Give the extent of all uninfected red blood cells.
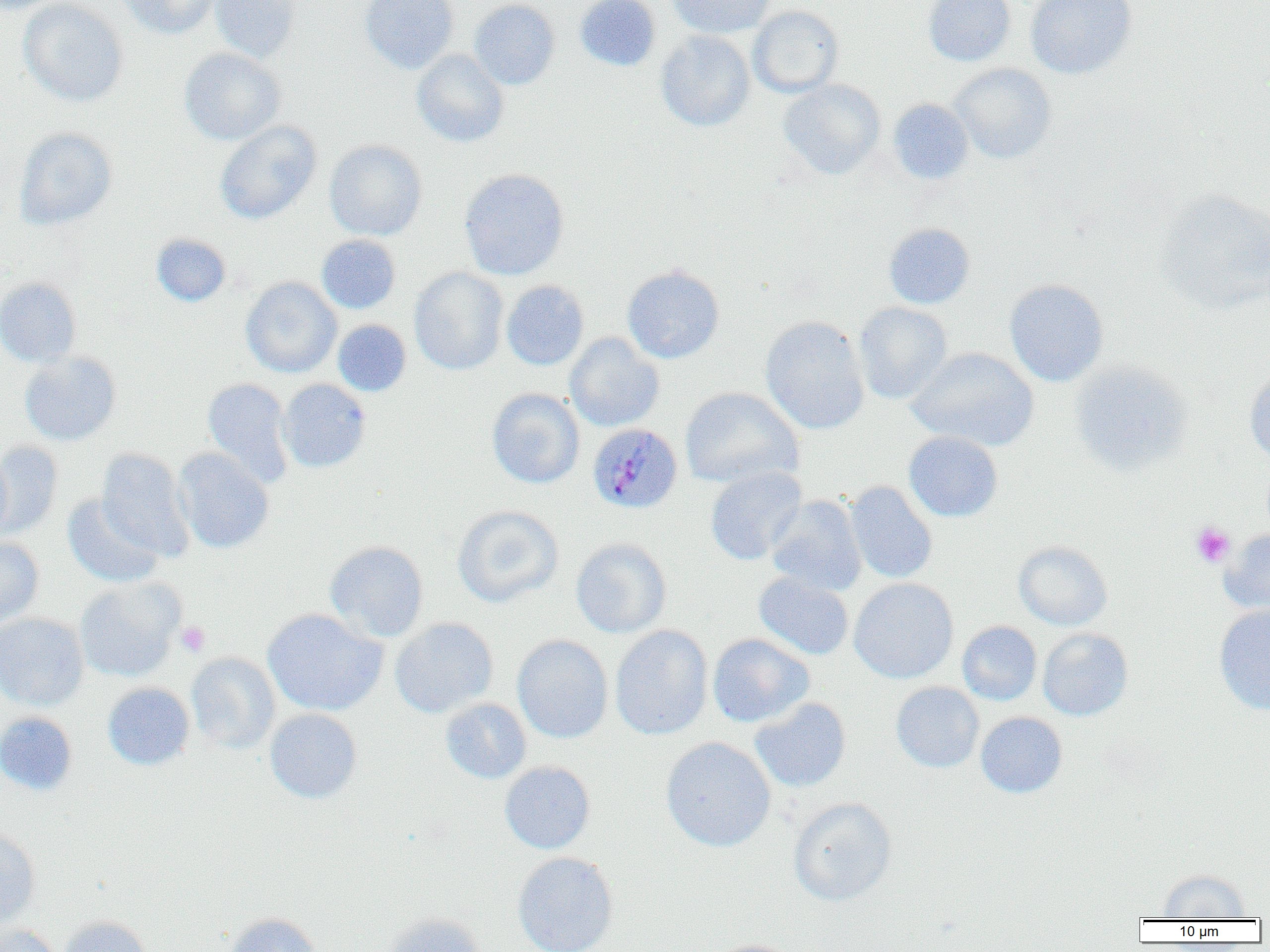
Approximate bounding boxes as [x1, y1, x2, y2] in pixels.
Uninfected red blood cells: [1, 0, 69, 14], [18, 0, 129, 107], [118, 0, 221, 39], [211, 0, 300, 62], [359, 0, 458, 73], [469, 0, 560, 89], [574, 0, 661, 71], [668, 0, 776, 38], [923, 0, 1016, 66], [1026, 0, 1137, 79], [748, 5, 844, 97], [656, 31, 755, 131], [179, 47, 285, 145], [411, 50, 508, 147], [948, 63, 1057, 164], [777, 79, 886, 180], [887, 98, 974, 185], [215, 120, 321, 224], [13, 127, 118, 230], [324, 139, 427, 240], [459, 168, 570, 280], [1155, 189, 1270, 313], [883, 222, 975, 309], [150, 233, 231, 306], [316, 234, 401, 314], [622, 265, 725, 363], [409, 267, 509, 375], [0, 277, 81, 367], [241, 277, 342, 377], [1004, 279, 1108, 386], [501, 280, 589, 370], [853, 302, 953, 404], [760, 316, 869, 434], [333, 319, 411, 396], [564, 333, 664, 431], [906, 347, 1039, 451], [19, 351, 121, 446], [1069, 361, 1194, 475], [1245, 369, 1270, 468], [202, 378, 295, 488], [277, 378, 371, 473], [680, 387, 804, 489], [486, 388, 585, 488], [904, 431, 1003, 522], [0, 441, 62, 537], [97, 447, 195, 562], [0, 448, 12, 542], [173, 448, 274, 553], [705, 466, 807, 565], [844, 481, 937, 583], [62, 494, 164, 587], [766, 495, 867, 595], [452, 505, 563, 608], [1220, 529, 1270, 614], [0, 537, 44, 630], [570, 537, 672, 638], [325, 540, 429, 642], [1013, 541, 1113, 631], [753, 572, 854, 660], [849, 577, 958, 683], [75, 578, 183, 681], [1214, 604, 1270, 714], [261, 608, 388, 716], [0, 612, 89, 711], [390, 617, 498, 718], [957, 621, 1042, 705], [609, 625, 713, 740], [1037, 628, 1133, 721], [707, 633, 814, 727], [512, 634, 613, 743], [186, 651, 281, 754], [891, 681, 984, 773], [102, 682, 195, 770], [750, 697, 851, 792], [440, 698, 532, 783], [264, 708, 362, 804], [0, 711, 77, 795], [975, 712, 1067, 798], [660, 736, 776, 852], [499, 761, 595, 854], [788, 797, 897, 906], [0, 829, 41, 927], [512, 852, 619, 952], [1157, 870, 1251, 919], [223, 912, 323, 952], [381, 912, 487, 952], [57, 916, 151, 952], [0, 923, 61, 952], [707, 939, 803, 952].

Summary:
  - Plasmodium malariae-infected red blood cell locations: [587, 421, 684, 514]
  - Platelet locations: [1191, 522, 1235, 568], [176, 620, 211, 657]
  - Slide-level diagnosis: Plasmodium malariae
  - Modality: light microscopy
  - Magnification: 1000x
  - Field of view: single
  - Preparation: thin blood smear
  - Image size: 1270×952 pixels